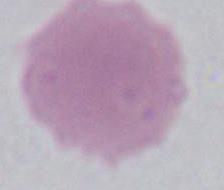

Summary:
  - Modality: photomicrograph
  - Magnification: 1000x
  - Identification: erythrocyte